State which cell type is depicted.
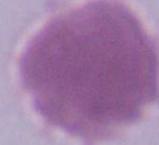

This is an erythrocyte.

magnification = 1000x
modality = photomicrograph